Classify this cell by malaria status.
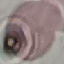
Uninfected.

Summary:
  - Image type: automatically extracted cell patch, resized to 64 × 64 pixels
  - Preparation: thin blood film
  - Capture: smartphone camera at the microscope eyepiece
  - Stain: Giemsa